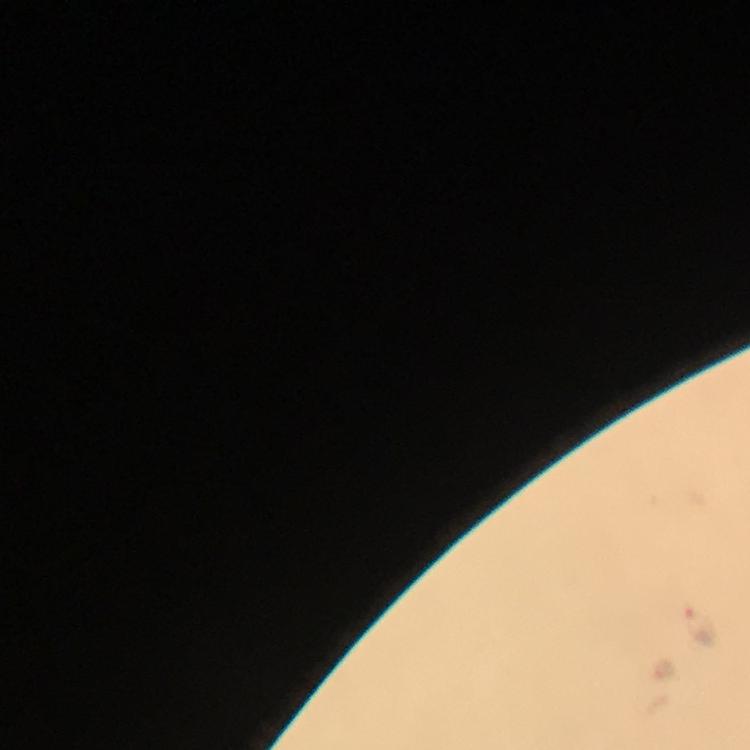

Approximate centers as [x, y] in pixels.
Summary:
  - Malaria parasite locations: [698, 625], [664, 670]
  - Immersion oil: used
  - Preparation: thick blood smear
  - Context: from a diagnostic examination for malaria
  - Capture: smartphone mounted on the microscope
  - Magnification: 100x
  - Stain: Giemsa
  - Cropped from: one field of view
  - Image size: 750×750 pixels